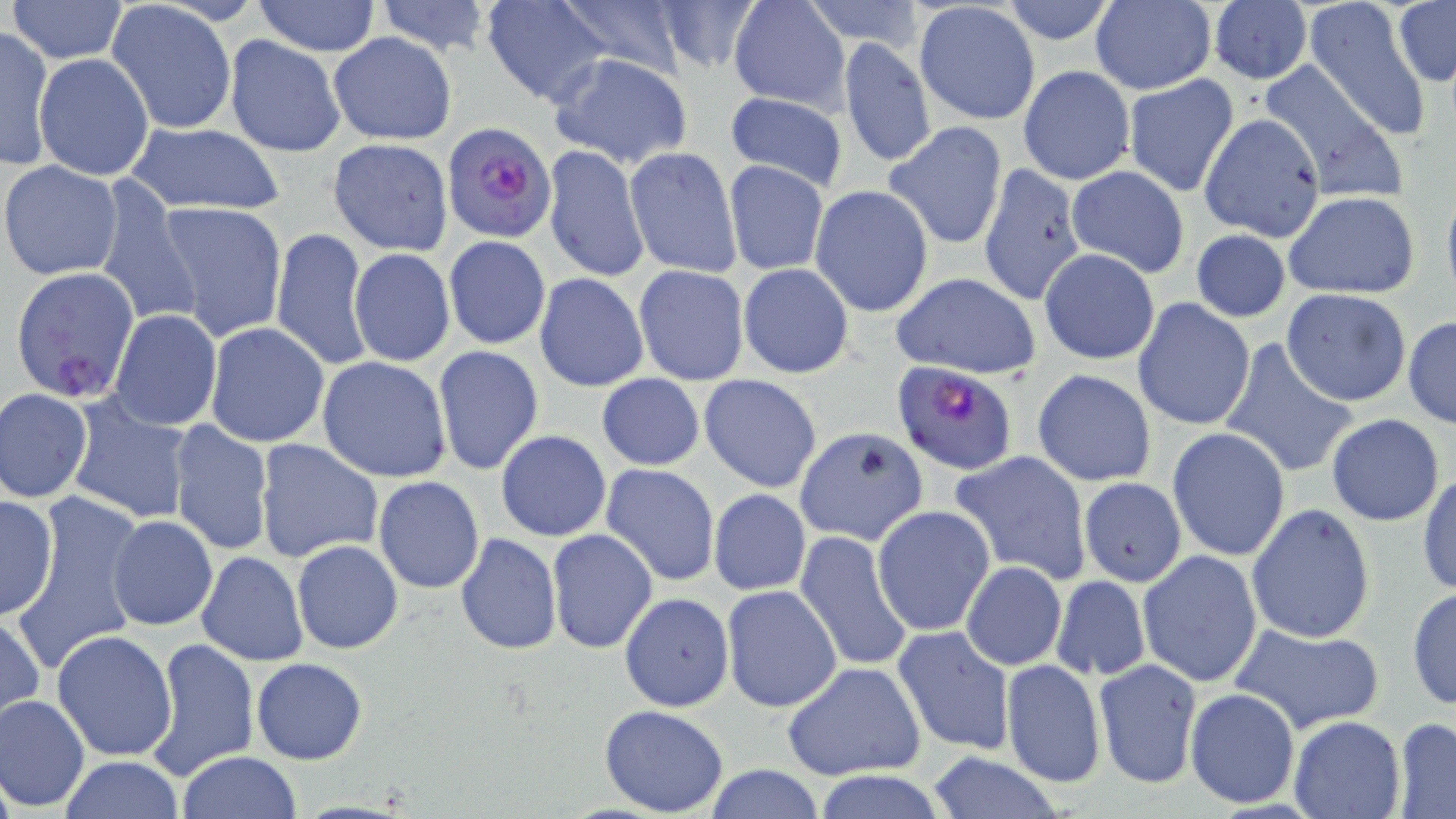

Summary:
  - Coordinate format: approximate bounding boxes as (x1,y1)-(x2,y2) corner pairs in pixels
  - Uninfected red blood cell locations: (6,0)-(129,65), (374,0)-(494,56), (481,0)-(615,106), (550,0)-(694,77), (652,0)-(764,73), (999,0)-(1119,46), (1305,0)-(1433,143), (250,1)-(382,56), (728,1)-(849,112), (801,1)-(928,50), (105,2)-(235,133), (913,2)-(1040,126), (1089,2)-(1215,93), (1207,2)-(1312,86), (1393,2)-(1455,86), (0,26)-(53,170), (327,32)-(458,145), (224,34)-(346,158), (838,37)-(935,169), (547,53)-(694,168), (35,54)-(155,181), (1257,60)-(1405,203), (1018,65)-(1135,185), (1123,74)-(1239,197), (723,92)-(849,193), (1199,113)-(1326,241), (883,121)-(1008,250), (127,122)-(285,216), (327,138)-(454,254), (543,144)-(650,284), (624,147)-(741,278), (723,160)-(829,276), (0,161)-(124,280), (978,161)-(1087,306), (1064,164)-(1190,278), (94,181)-(203,332), (810,184)-(934,318), (1282,191)-(1421,300), (152,198)-(288,343), (272,227)-(371,372), (1190,229)-(1291,322), (443,235)-(551,350), (1038,247)-(1161,365), (349,249)-(456,366), (738,264)-(853,379), (632,265)-(749,387), (534,273)-(649,392), (890,274)-(1040,380), (1281,288)-(1413,406), (1132,297)-(1256,432), (108,310)-(222,431), (1403,315)-(1456,429), (203,323)-(330,448), (1223,343)-(1360,479), (433,345)-(544,475), (318,357)-(454,482), (1032,368)-(1156,487), (596,373)-(706,471), (699,374)-(823,492), (1,388)-(94,502), (65,395)-(195,526), (1326,414)-(1444,526), (167,421)-(274,558), (797,428)-(931,551), (1167,428)-(1290,561), (495,430)-(612,542), (255,440)-(385,566), (948,452)-(1090,585), (601,464)-(721,586), (1417,469)-(1455,597), (374,476)-(485,593), (1077,477)-(1187,587), (710,489)-(810,595), (7,493)-(149,672), (0,494)-(58,622), (1245,502)-(1377,644), (873,506)-(994,636), (107,515)-(218,631), (548,529)-(657,653), (795,530)-(913,671), (455,533)-(562,654), (292,540)-(403,653), (755,540)-(911,751), (1137,549)-(1263,688), (197,551)-(308,667), (960,561)-(1067,670), (1052,576)-(1150,681), (722,585)-(843,712), (1406,587)-(1456,710), (619,592)-(734,711), (1,610)-(44,725), (1230,620)-(1386,735), (892,626)-(1017,755), (51,629)-(179,762), (147,638)-(258,779), (252,658)-(368,764), (1093,658)-(1202,789), (1002,659)-(1105,788), (782,662)-(926,781), (1184,686)-(1301,810), (0,693)-(90,810), (599,705)-(729,816), (1287,716)-(1405,819), (1392,717)-(1456,817), (177,751)-(302,818), (926,751)-(1064,819), (59,756)-(184,818), (704,765)-(827,819), (814,772)-(950,819)
  - Plasmodium falciparum-infected red blood cell locations: (443,121)-(555,242), (9,265)-(142,401), (890,361)-(1020,476)
  - Slide-level diagnosis: Plasmodium falciparum
  - Preparation: thin blood film
  - Magnification: 1000x
  - Modality: optical microscopy
  - Field of view: single
  - Image size: 1456×819 pixels
  - Stain: May-Grünwald-Giemsa